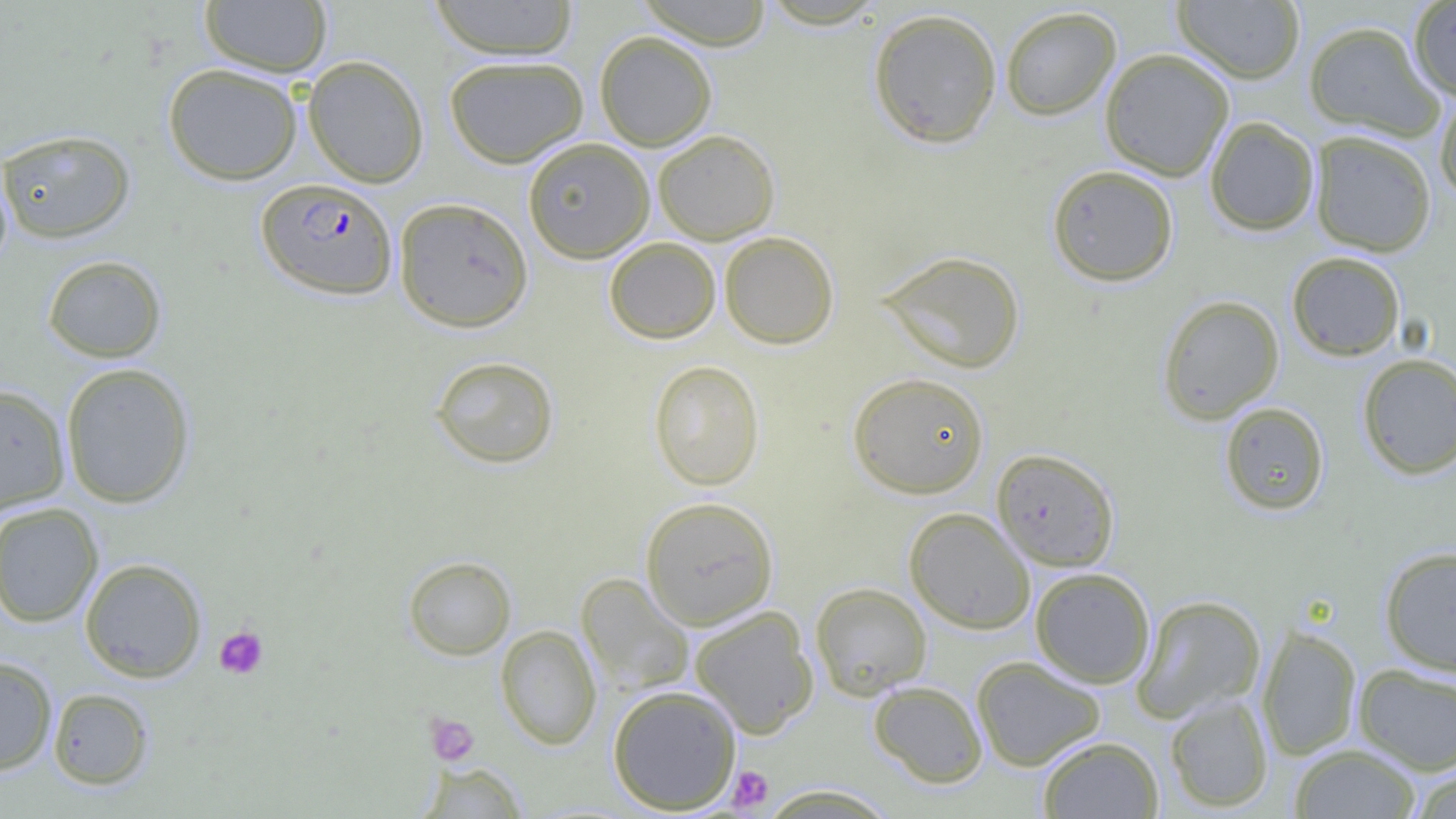
Plasmodium falciparum-infected red blood cell locations = approximate bounding boxes as [x1, y1, x2, y2] in pixels: [256, 178, 398, 300]
slide-level diagnosis = Plasmodium falciparum
image size = 1456×819 pixels
field of view = single
uninfected red blood cell locations = approximate bounding boxes as [x1, y1, x2, y2] in pixels: [199, 0, 333, 77], [427, 0, 581, 60], [635, 0, 775, 49], [1172, 0, 1305, 84], [1408, 1, 1456, 102], [999, 6, 1121, 121], [867, 7, 1003, 149], [1303, 20, 1444, 142], [594, 31, 717, 151], [1099, 47, 1234, 182], [303, 55, 429, 188], [444, 55, 589, 168], [163, 63, 303, 185], [1434, 89, 1456, 204], [1205, 116, 1319, 236], [0, 128, 136, 244], [653, 129, 780, 244], [1309, 130, 1437, 257], [522, 137, 655, 263], [1047, 164, 1178, 286], [394, 197, 533, 332], [719, 231, 839, 349], [604, 237, 721, 344], [876, 250, 1025, 374], [1286, 251, 1405, 361], [42, 255, 167, 363], [1156, 294, 1284, 424], [1357, 353, 1456, 480], [430, 355, 559, 469], [648, 359, 765, 490], [60, 362, 196, 509], [847, 371, 990, 498], [0, 383, 71, 513], [1219, 402, 1329, 515], [991, 448, 1120, 572], [640, 496, 779, 629], [0, 502, 103, 628], [904, 507, 1036, 634], [1379, 545, 1456, 676], [403, 555, 516, 660], [79, 557, 207, 683], [1029, 567, 1155, 688], [576, 573, 694, 697], [810, 582, 932, 700], [1131, 594, 1266, 723], [690, 605, 819, 738], [495, 624, 602, 749], [1256, 625, 1362, 760], [0, 656, 58, 775], [971, 656, 1105, 771], [1353, 664, 1456, 774], [868, 680, 988, 788], [607, 684, 742, 814], [48, 688, 154, 790], [1164, 693, 1274, 812], [1037, 735, 1165, 818], [1289, 743, 1422, 818], [417, 762, 529, 818], [1406, 765, 1456, 819], [755, 784, 900, 818]
magnification = 1000x
platelet locations = approximate bounding boxes as [x1, y1, x2, y2] in pixels: [214, 626, 268, 679], [426, 713, 479, 766], [727, 766, 774, 812]
modality = optical microscopy
preparation = thin blood smear